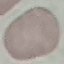
Summary:
  - Result: no malaria parasites seen
  - Preparation: thin smear
  - Stain: Giemsa
  - Capture: smartphone camera at the microscope eyepiece
  - Image type: cell patch, automatically extracted from a larger field of view and resized to 64 × 64 pixels